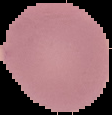

Summary:
  - Result: negative for Plasmodium parasites
  - Image type: segmented cell region with the area outside set to black
  - Image size: 112×115 pixels
  - Preparation: thin blood smear